State which parasite is depicted.
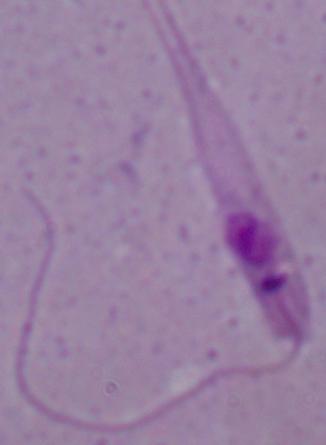

This is Leishmania.

Micrograph. Captured at 1000x magnification.